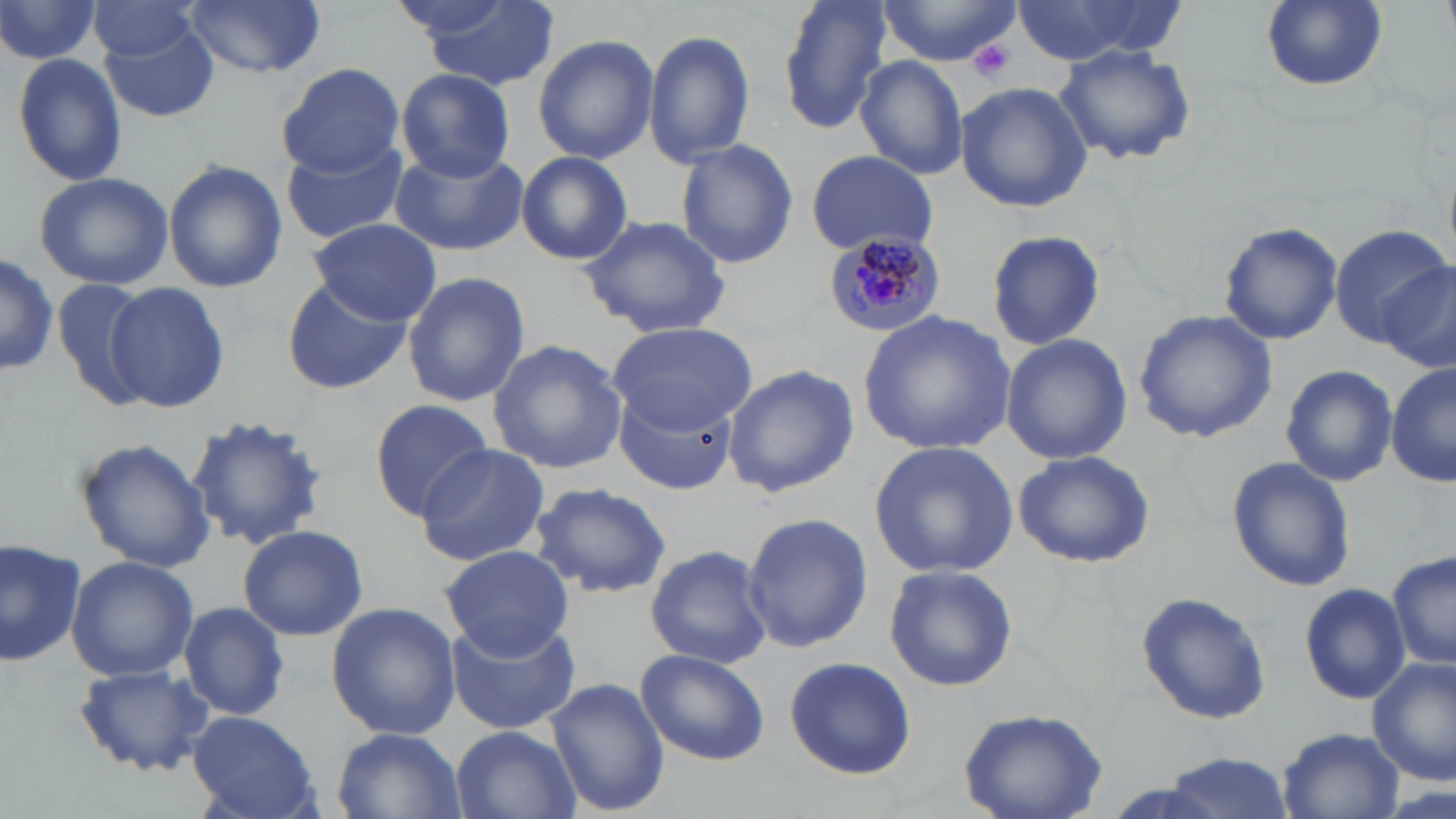

Summary:
  - Coordinate format: approximate bounding boxes as named x1/y1/x2/y2 corners in pixels
  - Platelet locations: (x1=968, y1=40, x2=1015, y2=82)
  - Plasmodium malariae-infected red blood cell locations: (x1=819, y1=231, x2=947, y2=341)
  - Uninfected red blood cell locations: (x1=0, y1=0, x2=103, y2=69), (x1=181, y1=0, x2=327, y2=76), (x1=404, y1=0, x2=565, y2=90), (x1=775, y1=0, x2=895, y2=130), (x1=875, y1=0, x2=1027, y2=66), (x1=1018, y1=0, x2=1182, y2=65), (x1=1260, y1=0, x2=1387, y2=92), (x1=87, y1=1, x2=205, y2=63), (x1=97, y1=19, x2=220, y2=123), (x1=643, y1=29, x2=756, y2=168), (x1=532, y1=33, x2=658, y2=165), (x1=1056, y1=45, x2=1195, y2=165), (x1=12, y1=52, x2=129, y2=187), (x1=853, y1=57, x2=971, y2=181), (x1=279, y1=63, x2=406, y2=176), (x1=397, y1=70, x2=515, y2=179), (x1=956, y1=82, x2=1093, y2=212), (x1=675, y1=138, x2=800, y2=267), (x1=282, y1=141, x2=408, y2=244), (x1=389, y1=145, x2=526, y2=254), (x1=805, y1=150, x2=940, y2=257), (x1=515, y1=151, x2=633, y2=265), (x1=163, y1=160, x2=288, y2=293), (x1=33, y1=171, x2=174, y2=291), (x1=579, y1=213, x2=733, y2=339), (x1=305, y1=219, x2=442, y2=326), (x1=1218, y1=221, x2=1343, y2=346), (x1=1331, y1=223, x2=1450, y2=349), (x1=985, y1=229, x2=1107, y2=352), (x1=0, y1=249, x2=57, y2=378), (x1=1377, y1=265, x2=1456, y2=370), (x1=402, y1=271, x2=530, y2=406), (x1=51, y1=277, x2=149, y2=410), (x1=282, y1=278, x2=412, y2=395), (x1=106, y1=280, x2=229, y2=415), (x1=1135, y1=309, x2=1278, y2=442), (x1=860, y1=312, x2=1015, y2=455), (x1=609, y1=323, x2=756, y2=432), (x1=999, y1=333, x2=1132, y2=466), (x1=486, y1=339, x2=628, y2=473), (x1=1279, y1=362, x2=1394, y2=487), (x1=722, y1=363, x2=858, y2=498), (x1=1387, y1=363, x2=1454, y2=489), (x1=616, y1=389, x2=735, y2=494), (x1=365, y1=400, x2=492, y2=519), (x1=186, y1=413, x2=330, y2=549), (x1=77, y1=438, x2=216, y2=574), (x1=869, y1=441, x2=1020, y2=578), (x1=414, y1=444, x2=550, y2=567), (x1=1011, y1=448, x2=1157, y2=569), (x1=1227, y1=458, x2=1356, y2=594), (x1=529, y1=481, x2=673, y2=599), (x1=740, y1=513, x2=874, y2=654), (x1=236, y1=523, x2=367, y2=641), (x1=0, y1=536, x2=89, y2=667), (x1=642, y1=544, x2=772, y2=670), (x1=437, y1=547, x2=576, y2=658), (x1=1388, y1=549, x2=1455, y2=673), (x1=65, y1=555, x2=199, y2=682), (x1=883, y1=565, x2=1020, y2=691), (x1=1299, y1=582, x2=1410, y2=705), (x1=1135, y1=592, x2=1273, y2=725), (x1=179, y1=601, x2=289, y2=720), (x1=325, y1=603, x2=461, y2=740), (x1=445, y1=615, x2=583, y2=733), (x1=634, y1=649, x2=769, y2=765), (x1=782, y1=656, x2=918, y2=779), (x1=1369, y1=657, x2=1455, y2=784), (x1=76, y1=663, x2=212, y2=777), (x1=546, y1=680, x2=669, y2=816), (x1=958, y1=705, x2=1112, y2=817), (x1=186, y1=711, x2=320, y2=819), (x1=450, y1=726, x2=581, y2=819), (x1=329, y1=728, x2=465, y2=819), (x1=1277, y1=728, x2=1403, y2=819), (x1=1158, y1=752, x2=1297, y2=819)
  - Slide-level diagnosis: Plasmodium malariae
  - Preparation: thin blood film
  - Modality: light microscopy
  - Stain: May-Grünwald-Giemsa
  - Magnification: 1000x
  - Field of view: one of a larger specimen
  - Image size: 1456×819 pixels